Classify this cell by malaria status.
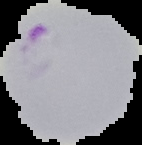
It is parasitized.

Summary:
  - Image type: segmented cell region on a black background
  - Image size: 142×145 pixels
  - Preparation: thin blood film